Report the malaria status.
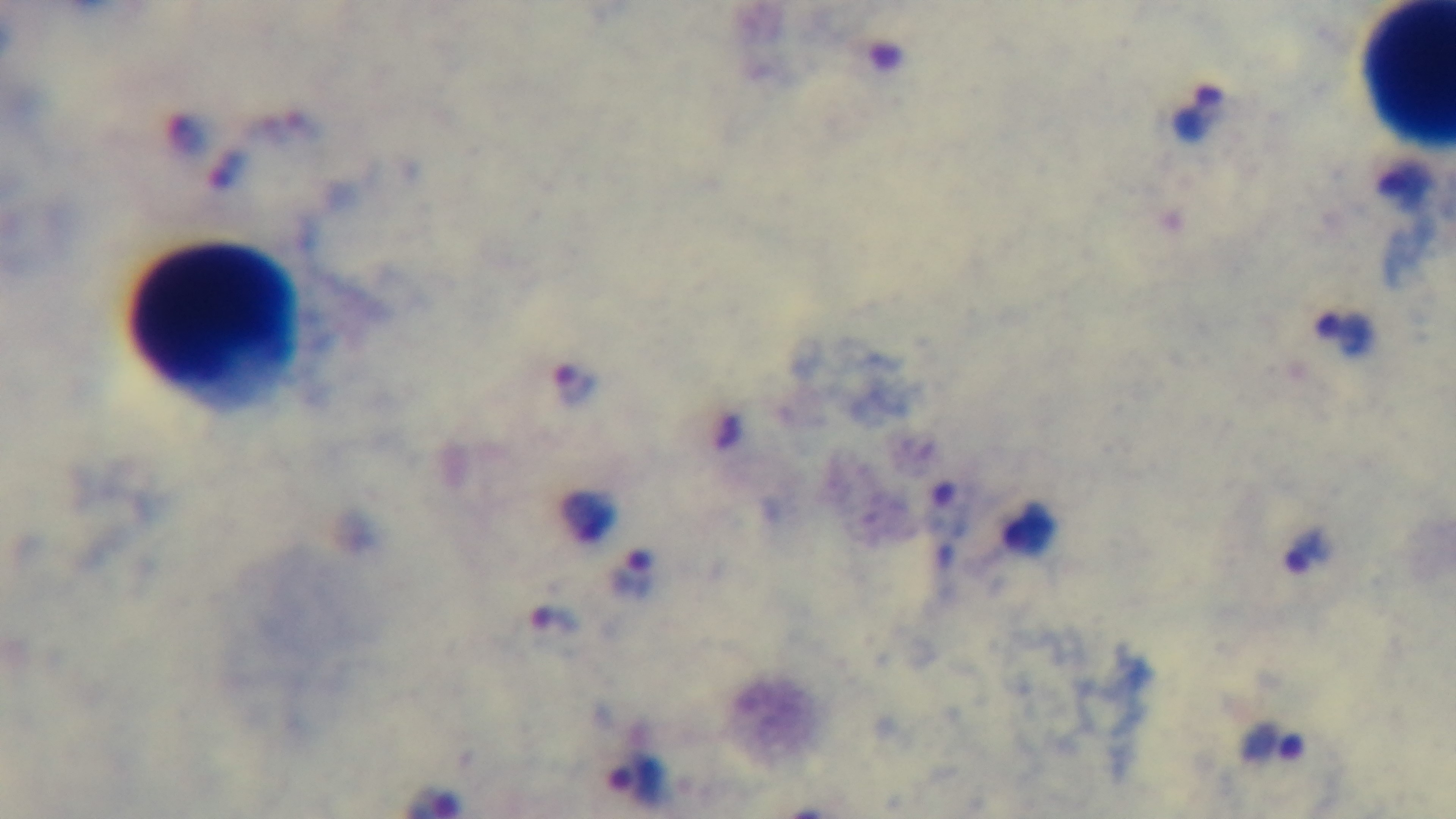

Positive.

One field from the slide. Preparation: thick smear. Giemsa-stained. Photomicrograph. Captured with a mounted 4K digital camera. Oil-immersion objective, 100x.